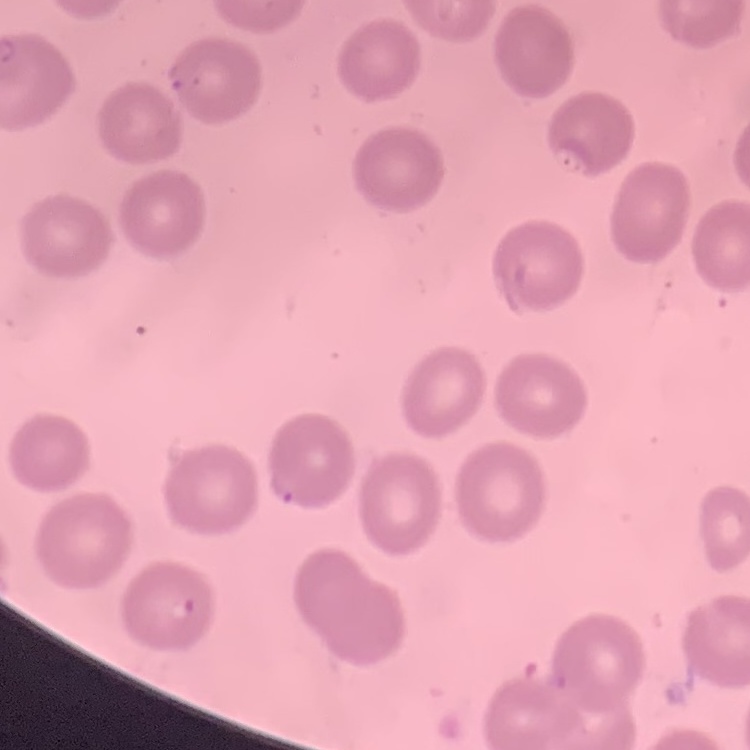

Summary:
  - Erythrocyte morphology: no rouleaux formation
  - Preparation: thin blood film
  - Image type: one tile cut from a larger photomicrograph
  - Stain: Field's or Giemsa